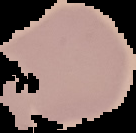
Summary:
  - Image type: segmented cell region with the area outside set to black
  - Image size: 136×133 pixels
  - Result: no malaria parasites detected
  - Preparation: thin blood smear